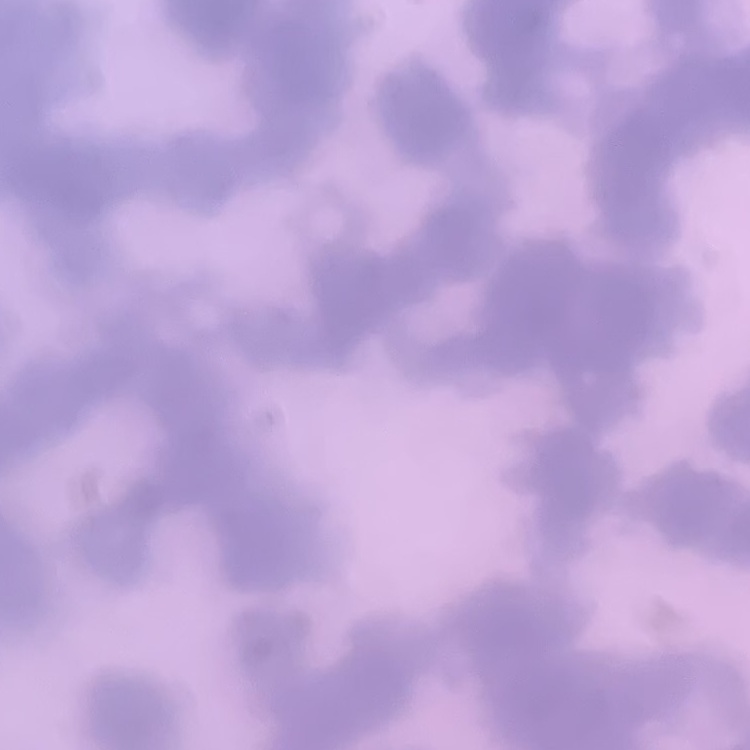
{
  "erythrocyte_morphology": "rouleaux formation",
  "stain": "Field's or Giemsa",
  "image_type": "one tile cut from a larger photomicrograph",
  "preparation": "thin blood film"
}